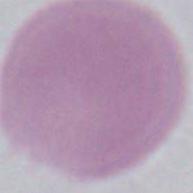
A red blood cell is shown. Micrograph. Captured at 1000x magnification.